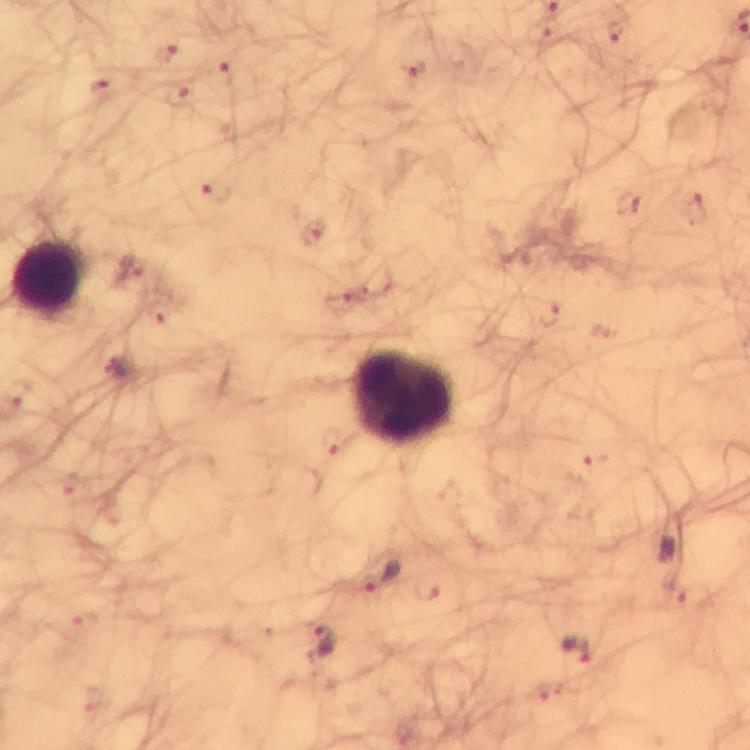
{
  "cropped_from": "a single field of view",
  "immersion_oil": "used",
  "preparation": "thick blood film",
  "capture": "smartphone photograph through a microscope",
  "leukocyte_locations": "approximate centers as {x, y} in pixels: {50, 279}, {404, 397}",
  "stain": "Giemsa",
  "plasmodium_parasite_locations": "approximate centers as {x, y} in pixels: {669, 547}, {383, 576}, {322, 643}, {578, 651}",
  "magnification": "100x",
  "context": "from a malaria diagnostic workup",
  "image_size": "750×750 pixels"
}